Assess this cell for malaria.
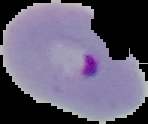

It is parasitized.

Segmented cell region on a black background. From a thin blood smear. Image is 148×124 pixels.